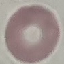
Summary:
  - Malaria status: uninfected
  - Stain: Giemsa
  - Image type: cell patch, automatically extracted from a larger field of view and resized to 64 × 64 pixels
  - Capture: smartphone camera at the microscope eyepiece
  - Preparation: thin smear